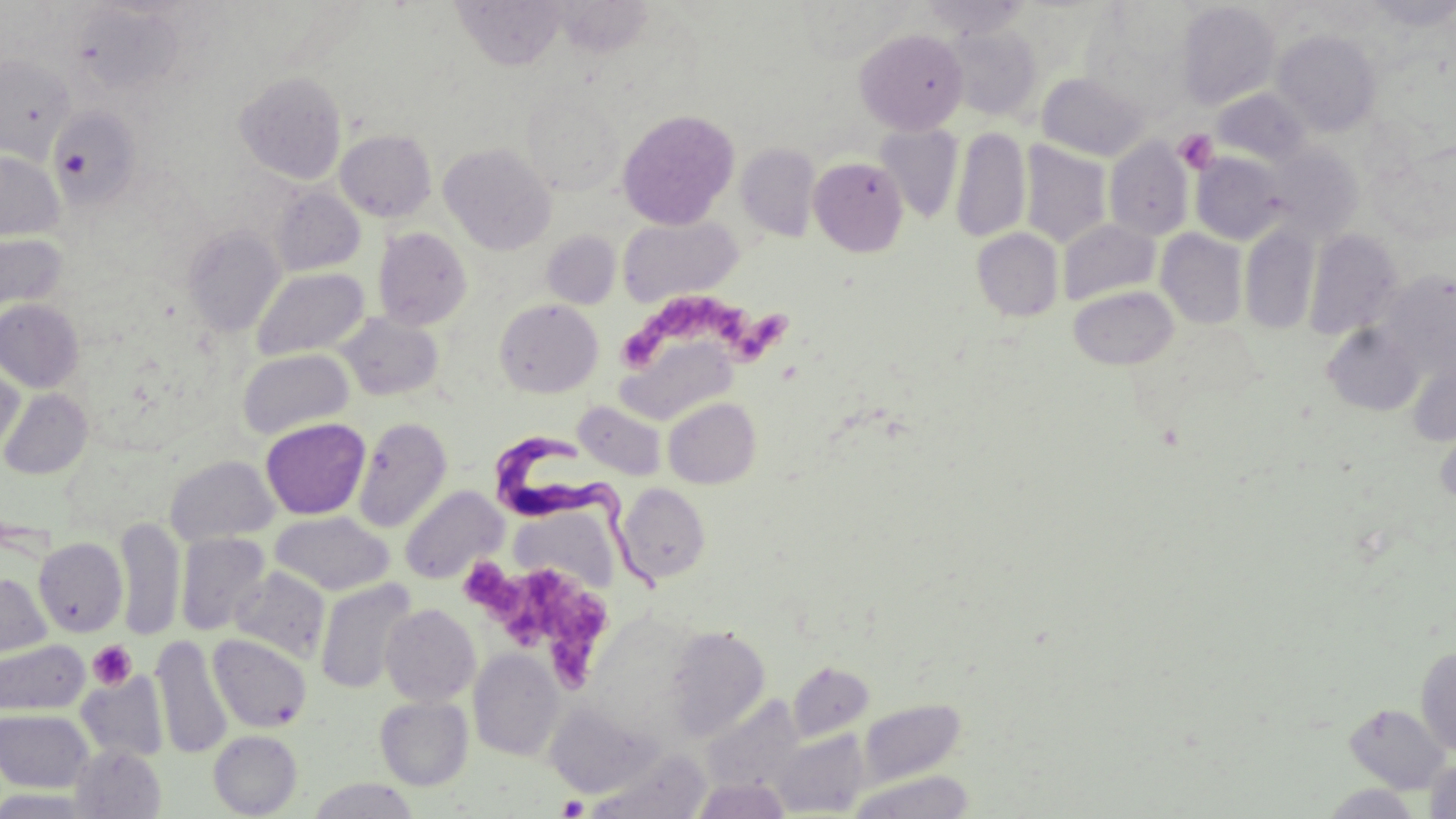

Summary:
  - Coordinate format: approximate bounding boxes as [x1, y1, x2, y2] in pixels
  - Platelet locations: [1174, 129, 1219, 174], [623, 293, 735, 364], [732, 310, 791, 363], [467, 561, 611, 684], [88, 639, 137, 690], [557, 796, 588, 818]
  - Uninfected red blood cell locations: [453, 0, 566, 70], [918, 0, 1035, 39], [1364, 0, 1456, 29], [555, 1, 655, 57], [792, 1, 916, 63], [1175, 2, 1281, 111], [70, 4, 187, 95], [946, 24, 1041, 121], [1084, 24, 1195, 122], [855, 28, 968, 133], [1272, 29, 1382, 135], [0, 53, 75, 160], [235, 71, 347, 184], [1036, 71, 1149, 160], [1213, 88, 1313, 167], [521, 89, 624, 197], [48, 107, 142, 209], [617, 109, 740, 229], [874, 123, 964, 224], [951, 126, 1030, 243], [335, 129, 437, 221], [1104, 136, 1194, 240], [1018, 141, 1113, 248], [439, 143, 556, 254], [736, 143, 821, 241], [1266, 146, 1364, 240], [0, 150, 63, 241], [1191, 151, 1289, 244], [809, 157, 908, 256], [271, 186, 365, 275], [618, 215, 743, 307], [1058, 219, 1160, 305], [183, 225, 285, 336], [1239, 225, 1319, 334], [373, 227, 472, 330], [972, 228, 1064, 322], [1156, 229, 1248, 329], [1305, 229, 1402, 340], [541, 230, 621, 309], [0, 232, 68, 312], [252, 267, 369, 361], [1378, 272, 1456, 376], [1069, 285, 1179, 369], [494, 298, 603, 397], [0, 299, 83, 392], [337, 313, 444, 400], [1322, 323, 1423, 415], [617, 336, 736, 425], [237, 348, 354, 440], [0, 358, 25, 455], [1406, 361, 1456, 446], [1, 388, 92, 479], [663, 397, 761, 488], [573, 401, 667, 480], [353, 416, 452, 532], [260, 418, 370, 519], [1434, 426, 1456, 509], [165, 455, 279, 546], [616, 483, 711, 585], [399, 485, 507, 584], [513, 510, 617, 593], [270, 511, 394, 596], [115, 517, 184, 640], [175, 532, 270, 636], [33, 537, 127, 637], [230, 567, 330, 662], [0, 572, 51, 661], [315, 579, 417, 694], [381, 604, 480, 707], [665, 625, 770, 740], [151, 634, 232, 760], [208, 634, 312, 733], [0, 639, 89, 715], [1416, 645, 1456, 756], [469, 648, 564, 761], [788, 661, 874, 742], [76, 673, 168, 763], [375, 696, 473, 790], [701, 696, 804, 794], [859, 699, 965, 786], [544, 700, 661, 798], [1344, 703, 1452, 793], [0, 709, 94, 792], [771, 729, 869, 815], [209, 730, 302, 817], [70, 745, 166, 819], [586, 750, 711, 819], [1424, 758, 1456, 818], [848, 770, 975, 819], [691, 777, 789, 819], [308, 778, 419, 819], [1321, 784, 1423, 818], [0, 789, 95, 818]
  - Trypanosoma brucei locations: [493, 428, 666, 596]
  - Slide-level diagnosis: Trypanosoma brucei
  - Modality: optical microscopy
  - Stain: May-Grünwald-Giemsa
  - Magnification: 1000x
  - Field of view: one of a larger specimen
  - Image size: 1456×819 pixels
  - Preparation: thin blood film